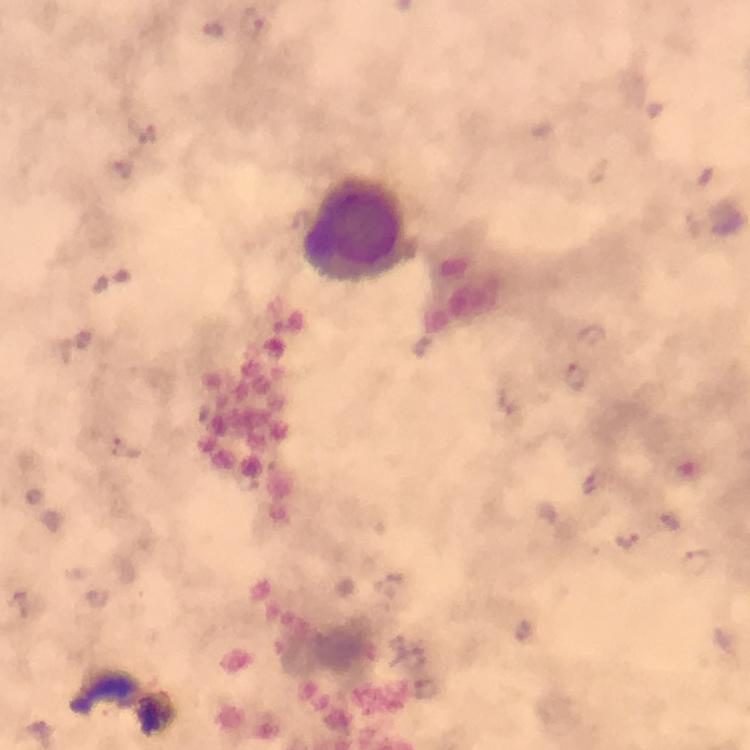
Approximate centers as (x, y) in pixels. Malaria parasite locations: (577, 377), (598, 484), (629, 540), (695, 562). Leukocyte locations: (354, 228). Smartphone photograph taken through a microscope. At 100x magnification. From a diagnostic examination for malaria. Image is 750×750 pixels. Immersion oil applied. Giemsa stain. Thick smear. A crop from one field of view.